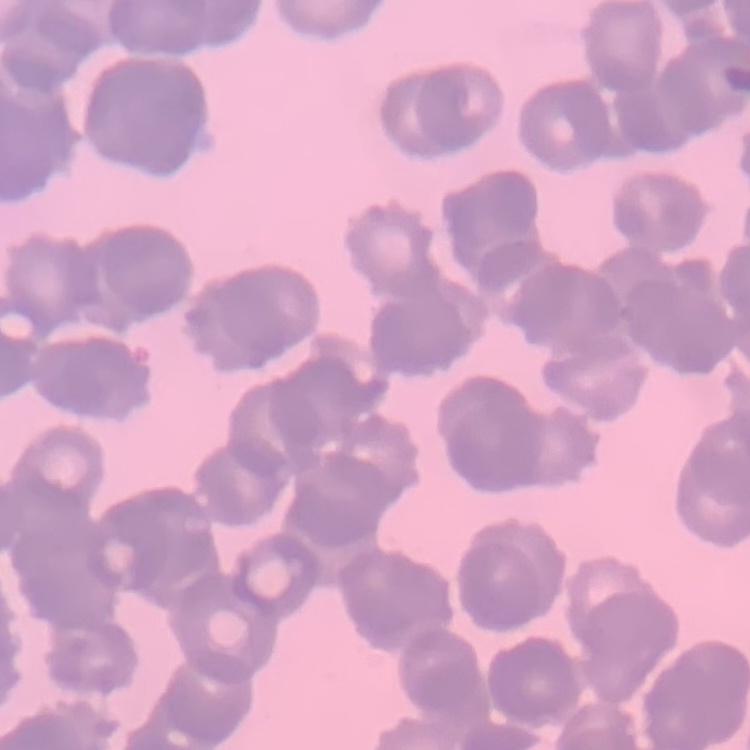
The red blood cells exhibit rouleaux formation. One tile cut from a larger photomicrograph. Thin peripheral smear. Field's or Giemsa stain.